Assess this cell for malaria.
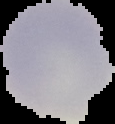
Uninfected.

image size = 115×124 pixels
image type = cell region segmented out of the field of view; surrounding area masked to black
preparation = thin blood smear